Locate every malaria parasite and identify its life-cycle stage.
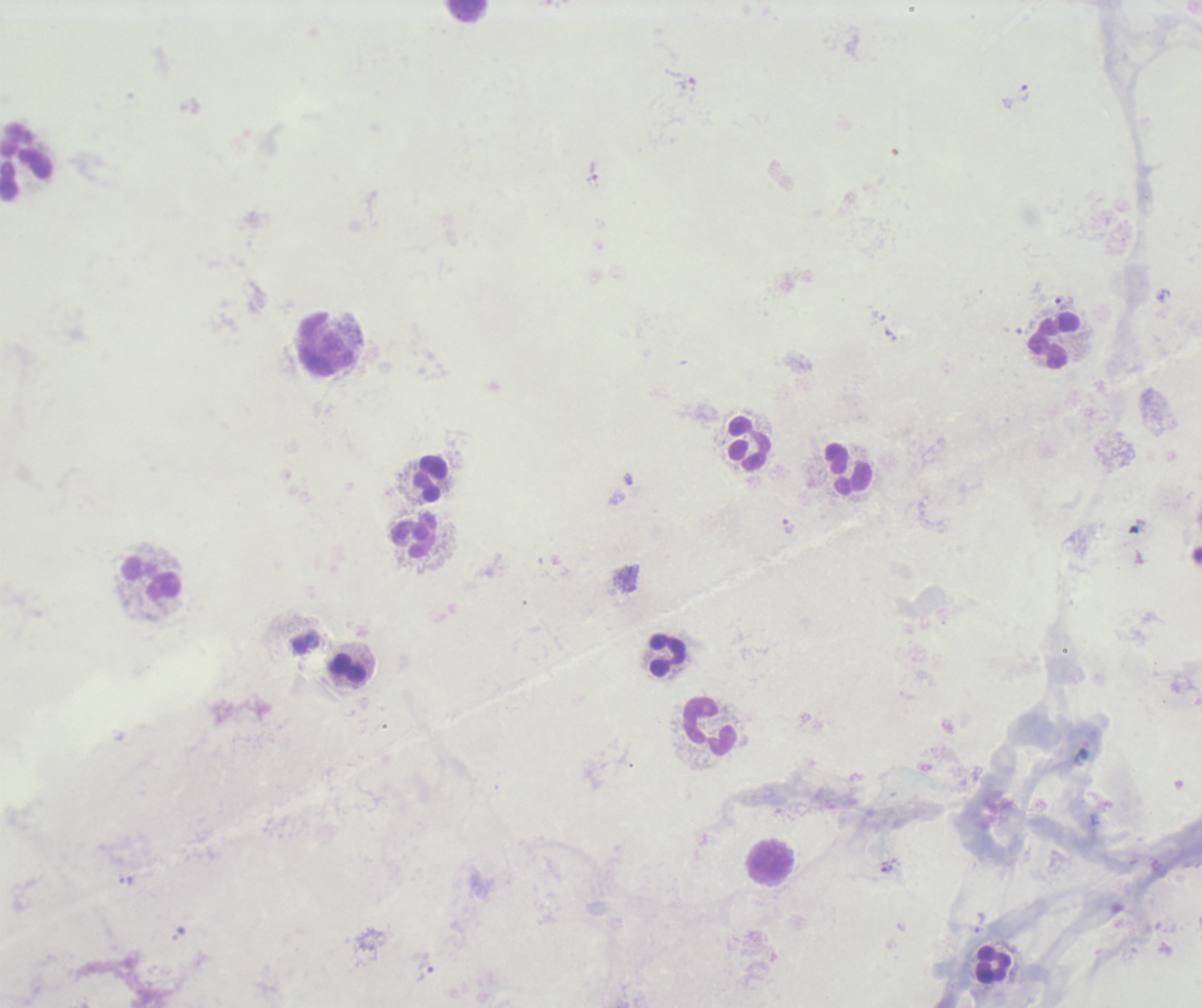

Approximate centers as (x, y) in pixels.
Trophozoites: (1023, 93), (592, 175), (1063, 302), (788, 527), (885, 868), (424, 966).
No schizont or gametocyte forms observed.

coordinate format = approximate centers as (x, y) in pixels
leukocyte locations = (467, 12), (26, 160), (1052, 341), (327, 344), (748, 444), (846, 469), (429, 479), (412, 537), (151, 579), (666, 656), (347, 669), (708, 727), (771, 864), (993, 965)
magnification = 100x
field of view = one from this slide
background quality = unsatisfactory
image size = 1202×1008 pixels
context = previously used in an actual diagnosis
stain = Romanowsky
preparation = thick blood film